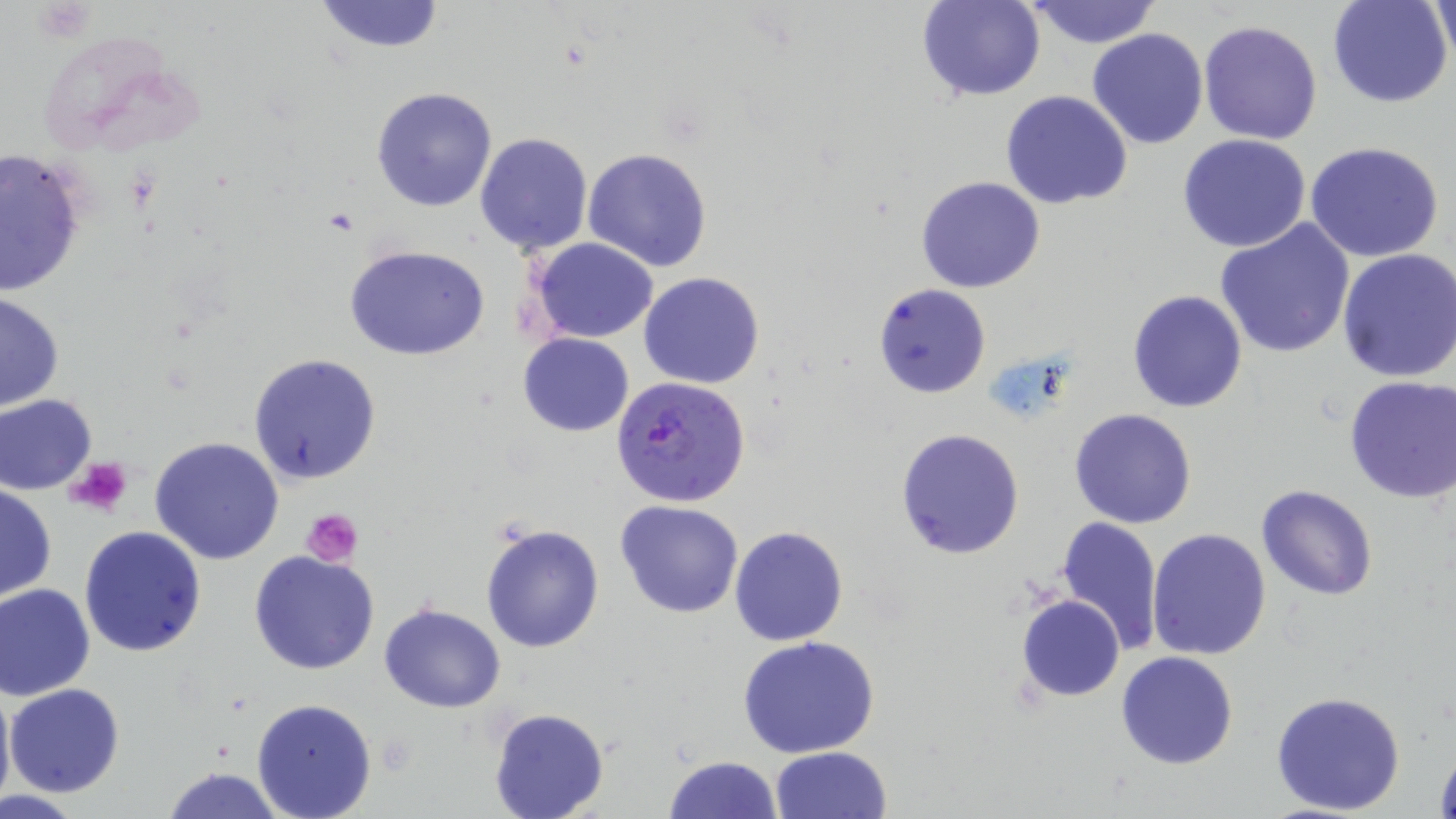
Summary:
  - Coordinate format: approximate bounding boxes as (x1, y1, x2, y2) in pixels
  - Uninfected red blood cell locations: (311, 0, 447, 53), (916, 0, 1045, 101), (1022, 0, 1163, 47), (1328, 0, 1455, 108), (1430, 0, 1455, 70), (1197, 19, 1323, 145), (1087, 28, 1210, 149), (370, 87, 498, 213), (1001, 91, 1132, 209), (475, 132, 593, 257), (1178, 134, 1312, 254), (1304, 142, 1446, 262), (0, 147, 89, 299), (582, 148, 713, 273), (916, 176, 1046, 293), (1215, 220, 1356, 360), (529, 237, 658, 343), (344, 244, 490, 361), (1336, 246, 1456, 383), (639, 272, 764, 388), (873, 284, 991, 399), (1127, 290, 1248, 412), (1, 292, 66, 414), (518, 333, 634, 436), (248, 352, 382, 486), (1343, 376, 1456, 503), (1, 394, 98, 495), (1068, 409, 1197, 529), (895, 428, 1024, 559), (149, 436, 285, 564), (0, 483, 56, 603), (1256, 485, 1378, 601), (615, 500, 744, 619), (1054, 516, 1163, 655), (479, 520, 605, 652), (78, 525, 207, 658), (729, 525, 849, 647), (1147, 529, 1273, 661), (248, 551, 380, 675), (0, 582, 96, 700), (1015, 594, 1125, 702), (380, 602, 506, 712), (737, 634, 883, 757), (1117, 650, 1238, 769), (0, 679, 15, 813), (6, 683, 125, 799), (1269, 689, 1407, 814), (250, 698, 377, 818), (488, 707, 610, 819), (1432, 740, 1456, 819), (770, 746, 892, 819), (663, 755, 785, 818), (162, 765, 288, 819)
  - Plasmodium falciparum-infected red blood cell locations: (611, 375, 751, 507)
  - Platelet locations: (66, 457, 134, 519), (301, 507, 364, 566)
  - Slide-level diagnosis: Plasmodium falciparum
  - Image size: 1456×819 pixels
  - Preparation: thin blood film
  - Stain: May-Grünwald-Giemsa
  - Magnification: 1000x
  - Field of view: one of a larger specimen
  - Modality: optical microscopy